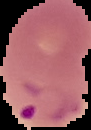

Summary:
  - Malaria status: parasitized
  - Image size: 91×130 pixels
  - Image type: segmented cell region with the area outside set to black
  - Preparation: thin blood smear